Report the malaria status of this cell.
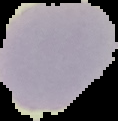

Uninfected.

Summary:
  - Preparation: thin blood smear
  - Image type: segmented cell region on a black background
  - Image size: 118×121 pixels